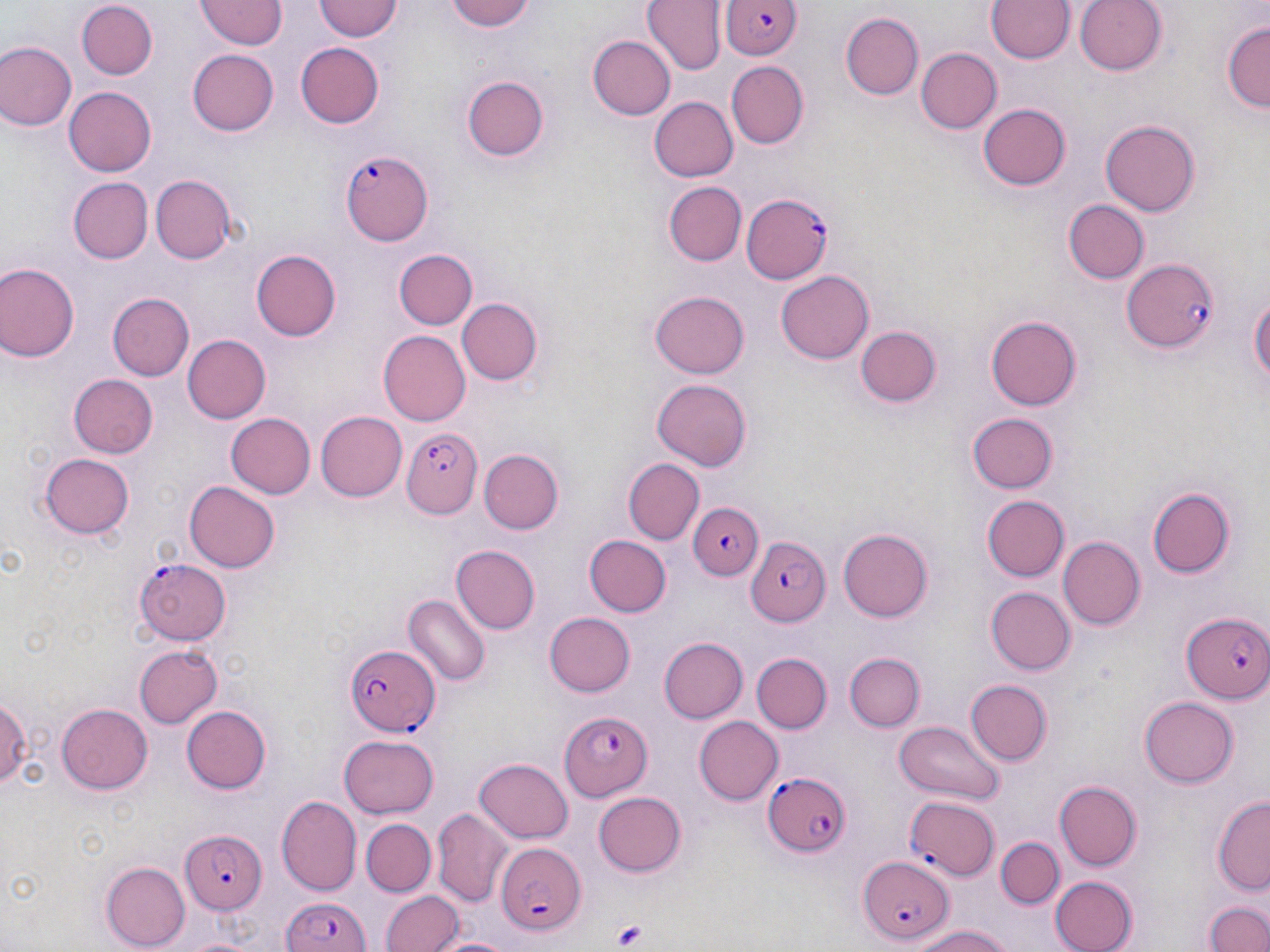
slide-level diagnosis = Plasmodium falciparum
modality = optical microscopy
field of view = single
uninfected red blood cell locations (subset) = approximate bounding boxes as (x1,y1)-(x2,y2) corner pairs in pixels: (313,0)-(402,42), (446,0)-(537,32), (1074,0)-(1166,76), (197,1)-(287,49), (644,1)-(725,75), (987,1)-(1073,64), (76,2)-(159,79), (841,11)-(924,100), (1222,19)-(1269,114), (586,35)-(675,121), (1,41)-(76,132), (296,42)-(384,129), (915,48)-(1001,134), (186,49)-(277,136), (725,62)-(810,149), (462,75)-(548,161), (64,87)-(156,176), (647,97)-(737,182), (978,102)-(1071,189), (1100,118)-(1200,218), (151,175)-(238,263), (68,178)-(153,263), (663,181)-(745,265), (1062,199)-(1149,284), (249,248)-(341,342), (393,248)-(478,330), (0,263)-(78,364), (775,270)-(874,365), (1247,285)-(1269,398), (108,291)-(194,381), (649,291)-(750,378), (456,297)-(543,386), (985,316)-(1083,410), (855,326)-(940,407), (377,330)-(469,426), (183,335)-(270,423), (69,375)-(157,457), (653,379)-(751,472), (313,412)-(406,502), (226,413)-(316,499), (966,413)-(1059,495), (478,449)-(561,535), (41,451)-(135,538), (623,458)-(702,544), (184,480)-(279,571), (1146,487)-(1234,579), (981,494)-(1068,582), (838,527)-(933,622), (584,534)-(671,617), (1058,536)-(1146,632), (452,545)-(539,634), (986,587)-(1075,674), (404,594)-(490,686), (544,613)-(636,697), (658,637)-(748,724), (134,644)-(221,728), (845,650)-(924,731), (752,652)-(830,734), (964,679)-(1051,768), (0,691)-(27,793), (1140,696)-(1237,787), (56,703)-(153,794), (181,705)-(271,794), (693,715)-(781,805), (892,717)-(1003,804), (341,732)-(439,816), (475,756)-(574,843), (1054,781)-(1143,868), (593,791)-(687,877), (1211,794)-(1270,893), (278,795)-(361,894), (431,807)-(512,903), (360,819)-(436,896), (996,837)-(1063,910), (100,862)-(190,948), (1049,874)-(1140,952), (381,890)-(462,952), (1205,898)-(1270,952), (909,925)-(1019,952), (428,932)-(519,952)
Plasmodium falciparum-infected red blood cell locations (subset) = approximate bounding boxes as (x1,y1)-(x2,y2) corner pairs in pixels: (722,0)-(801,60), (342,149)-(434,246), (740,191)-(832,283), (1121,258)-(1221,353), (402,428)-(481,519), (687,501)-(766,581), (744,537)-(829,627), (132,557)-(231,646), (1182,609)-(1270,702), (345,642)-(438,735), (561,709)-(653,803), (764,769)-(850,856), (180,829)-(268,915), (493,837)-(588,938), (857,853)-(953,945), (277,894)-(374,952)
preparation = thin blood smear
platelet locations = approximate bounding boxes as (x1,y1)-(x2,y2) corner pairs in pixels: (613,921)-(648,950)
magnification = 1000x
stain = May-Grünwald-Giemsa
image size = 1270×952 pixels